Assess this cell for malaria.
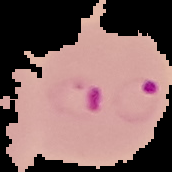

Parasitized.

Summary:
  - Preparation: thin blood film
  - Image size: 172×172 pixels
  - Image type: cell region segmented out of the field of view; surrounding area masked to black